Report the malaria status of this cell.
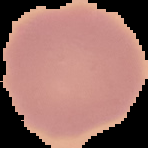

Uninfected.

Image is 148×148 pixels. From a thin blood film. Cell region segmented out of the field of view; the surrounding area is masked to black.